Assess this cell for malaria.
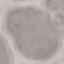

Uninfected.

Acquired by smartphone through the microscope eyepiece. Automatically extracted cell patch, resized to 64 × 64 pixels. Giemsa stain. Thin smear of blood.